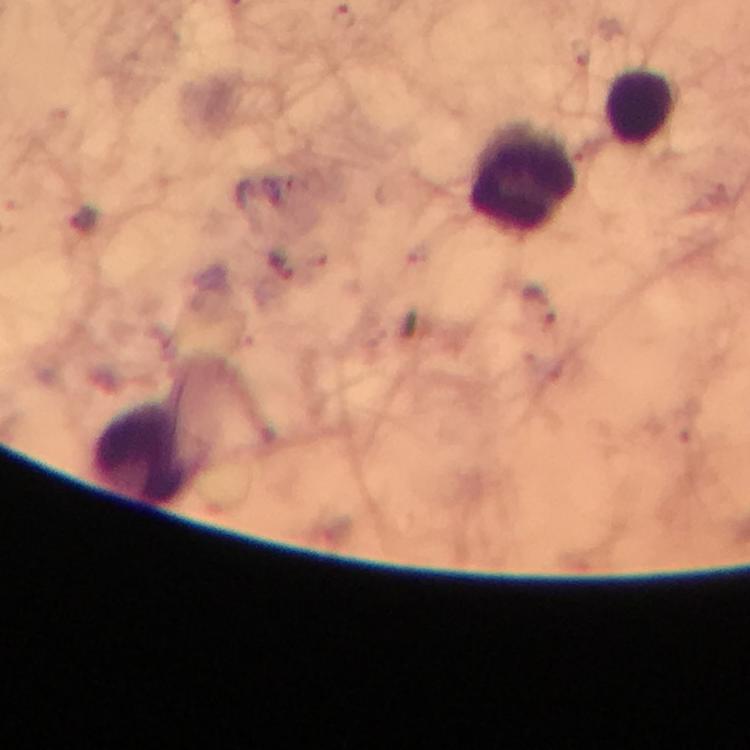

{
  "image_size": "750×750 pixels",
  "context": "from a diagnostic examination for malaria",
  "preparation": "thick smear",
  "malaria_parasites": "none seen",
  "cropped_from": "a single field of view",
  "capture": "smartphone camera through the microscope",
  "immersion_oil": "applied",
  "leukocyte_locations": "approximate centers as [x, y] in pixels: [644, 107], [521, 178], [146, 454]",
  "stain": "Giemsa",
  "magnification": "100x"
}